Outline each Plasmodium ovale-infected red blood cell.
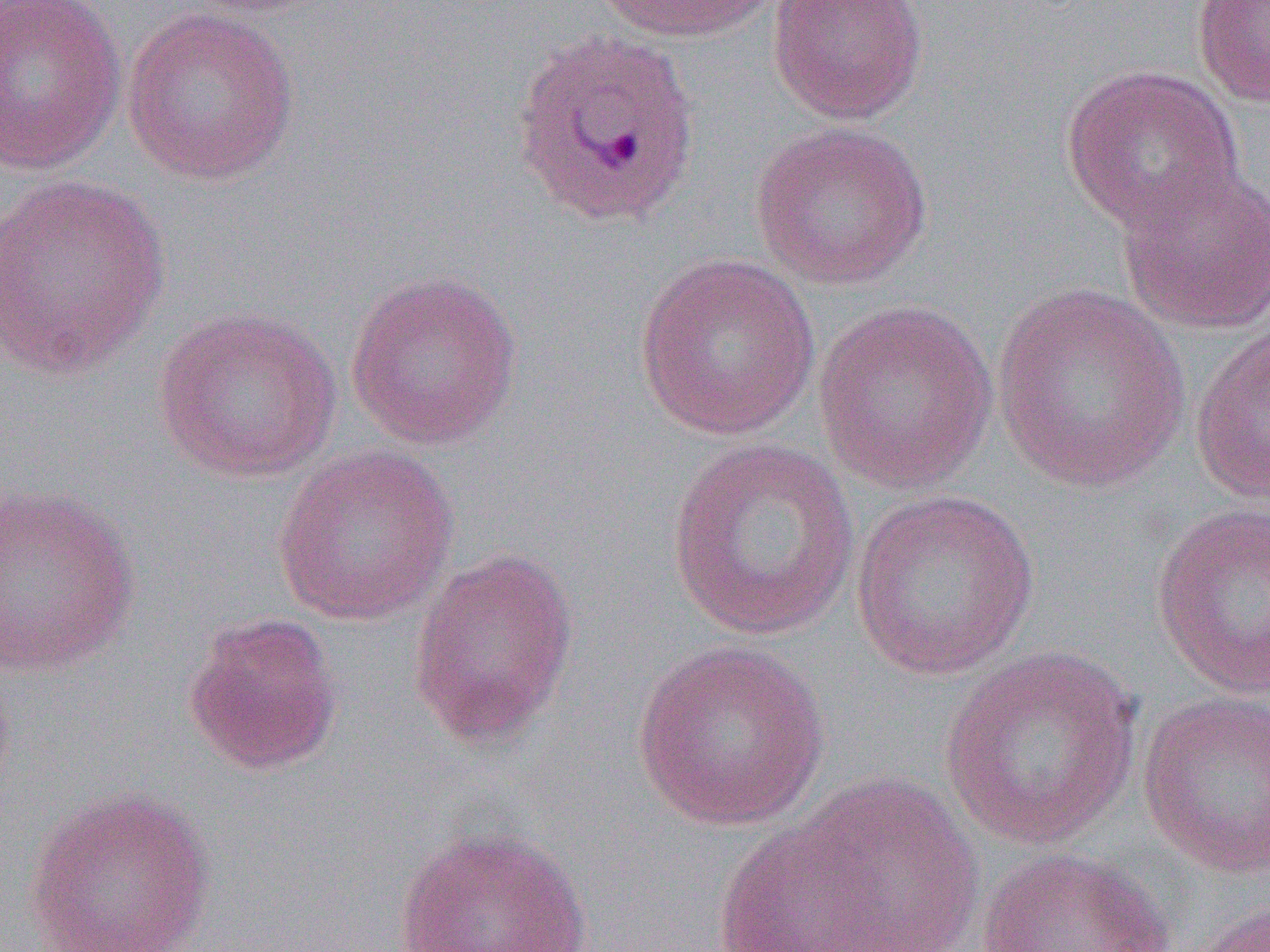
Approximate bounding boxes as (x1,y1)-(x2,y2) corner pairs in pixels.
Plasmodium ovale-infected red blood cells: (510,26)-(702,233).

Summary:
  - Uninfected red blood cell locations: (0,0)-(128,175), (178,0)-(344,19), (591,0)-(784,43), (766,0)-(929,125), (1191,0)-(1270,107), (121,7)-(299,187), (1060,63)-(1243,236), (749,120)-(934,291), (1114,158)-(1270,337), (0,173)-(171,382), (633,251)-(822,442), (345,269)-(524,450), (992,284)-(1191,495), (812,299)-(999,498), (151,306)-(342,482), (1189,323)-(1269,505), (666,437)-(858,642), (271,443)-(460,626), (0,484)-(142,678), (849,487)-(1040,680), (1150,502)-(1270,699), (407,547)-(581,749), (181,612)-(344,776), (630,639)-(832,831), (938,646)-(1144,850), (0,656)-(18,806), (1137,691)-(1270,879), (784,772)-(985,952), (22,787)-(217,952), (708,821)-(892,952), (391,824)-(595,952), (973,846)-(1179,952), (1186,899)-(1270,952)
  - Slide-level diagnosis: Plasmodium ovale
  - Magnification: 1000x
  - Field of view: single
  - Image size: 1270×952 pixels
  - Modality: optical microscopy
  - Preparation: thin blood film